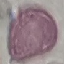

Summary:
  - Malaria status: uninfected
  - Preparation: thin blood film
  - Image type: cell patch, automatically extracted from a larger field of view and resized to 64 × 64 pixels
  - Capture: smartphone through the microscope eyepiece
  - Stain: Giemsa